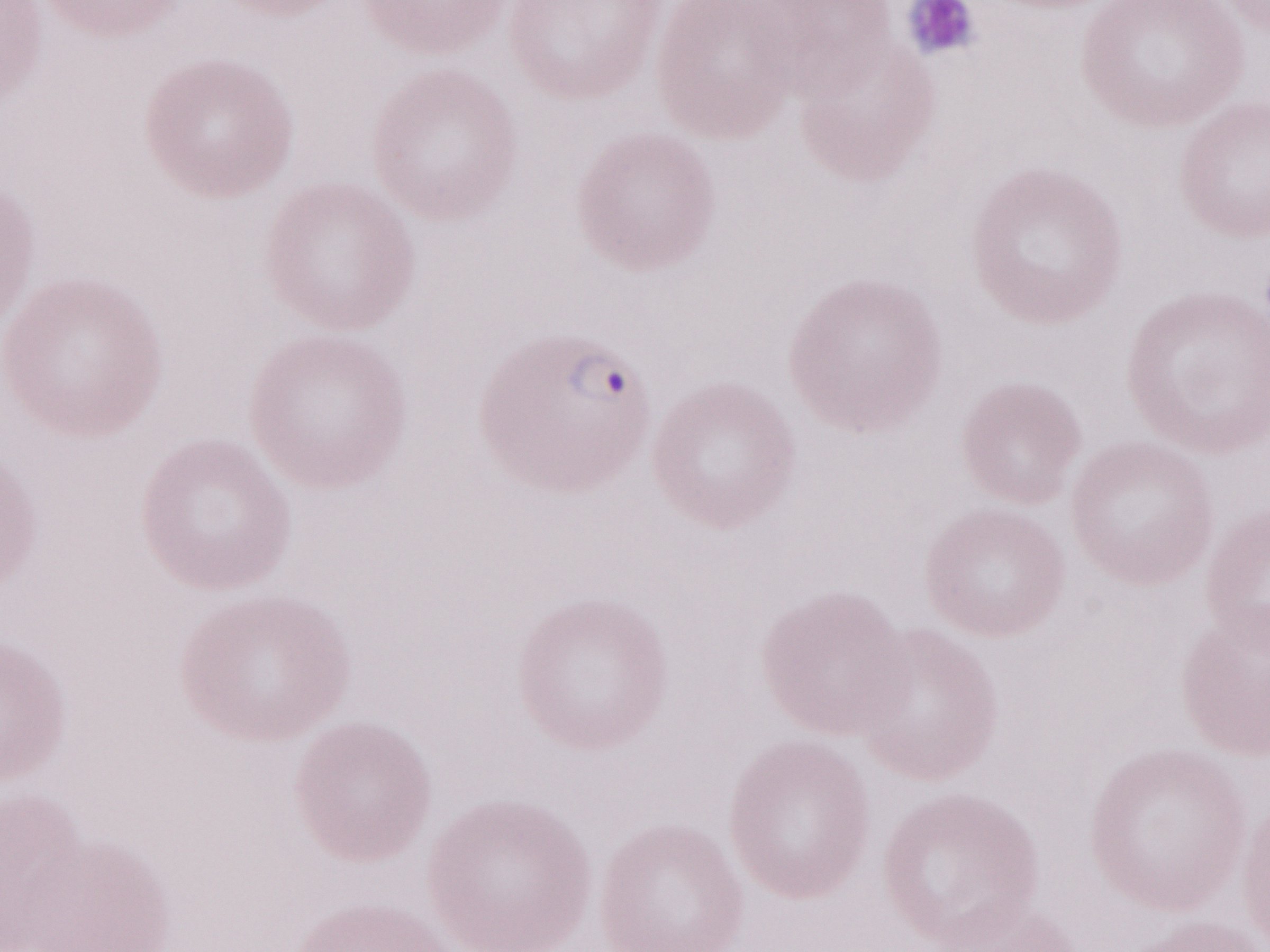
Patient diagnosis: malaria infection. May-Grünwald-Giemsa (MGG) stain. Olympus BX43 microscope, Olympus DP73 camera. One field of this slide. Image is 1270×952 pixels. Magnification: 1,000x. Thin peripheral-blood smear.